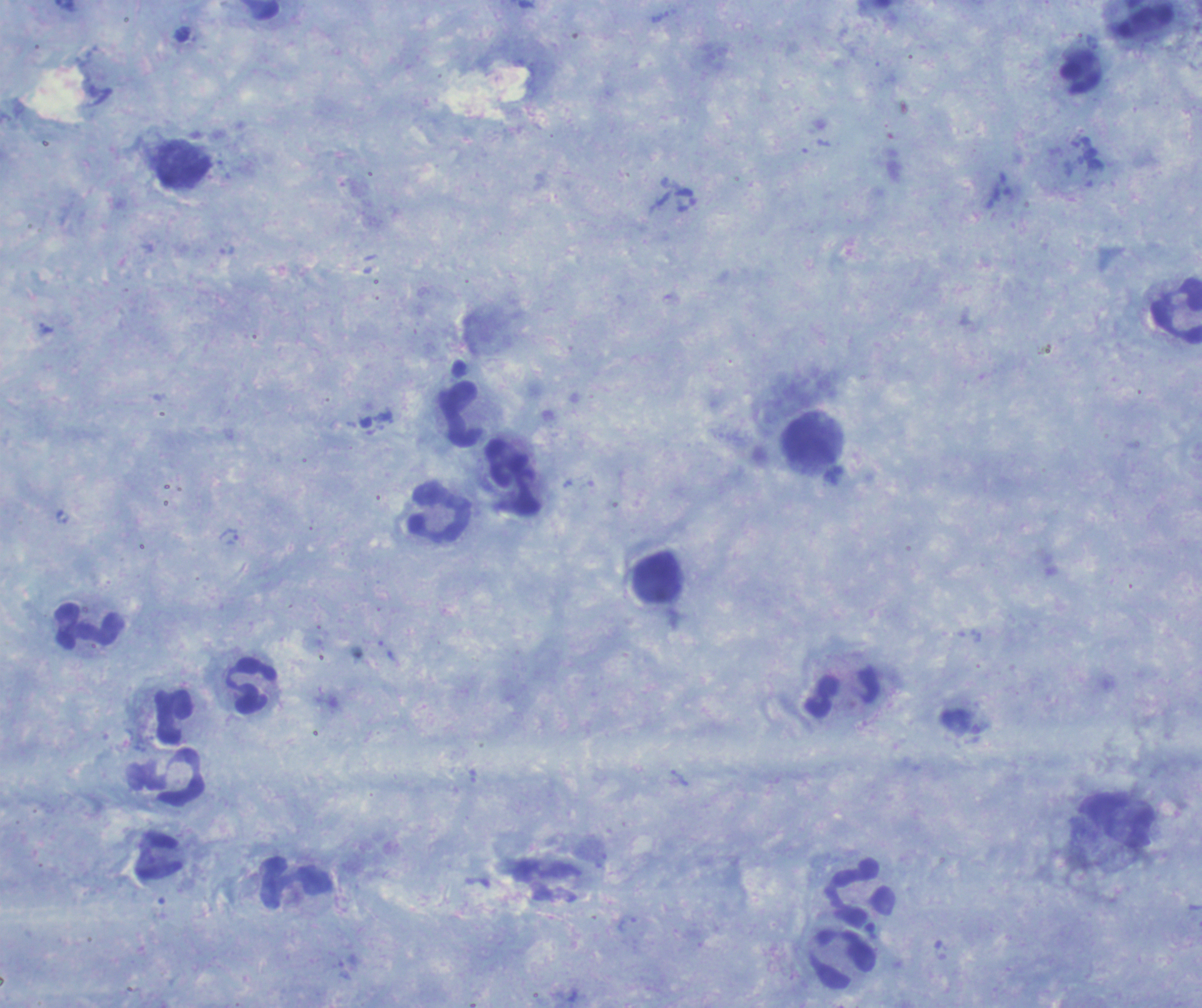

coordinate format = approximate centers as (x, y) in pixels
leukocyte locations = (1177, 312), (460, 413), (813, 440), (512, 477), (440, 514), (659, 578), (88, 626), (251, 686), (843, 693), (174, 715), (182, 778), (159, 856), (297, 882), (861, 892), (842, 958)
trophozoite locations = (230, 537)
preparation = thick blood film
stain = Romanowsky
field of view = one from this slide
magnification = 100x
context = previously used in an actual diagnosis
background quality = satisfactory
image size = 1202×1008 pixels
result = malaria parasites detected
coloration quality = good